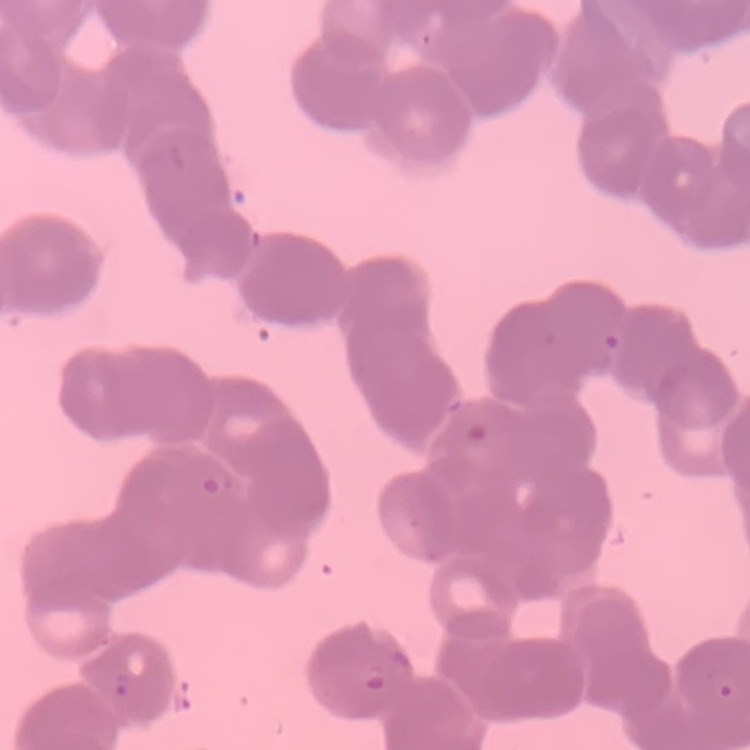

Summary:
  - Red blood cell morphology: rouleaux formation
  - Image type: one tile cut from a larger photomicrograph
  - Preparation: thin blood film
  - Stain: Field's or Giemsa